State the preparation type.
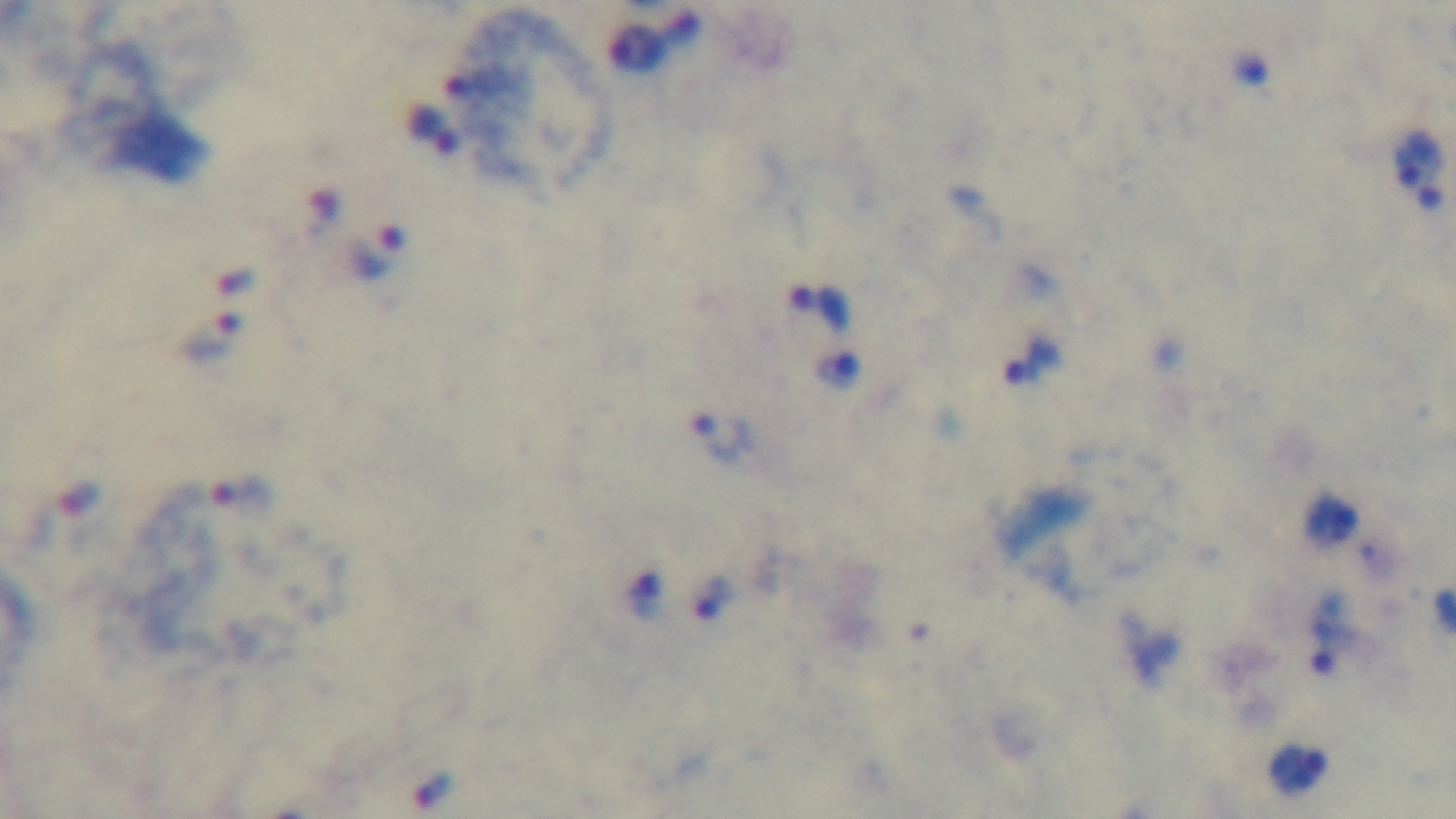

Thick.

Single field of view. 100x oil-immersion objective. Captured with a mounted 4K digital camera. Malaria status: infected. Giemsa-stained. Light microscopy.